Look for parasitized red blood cells.
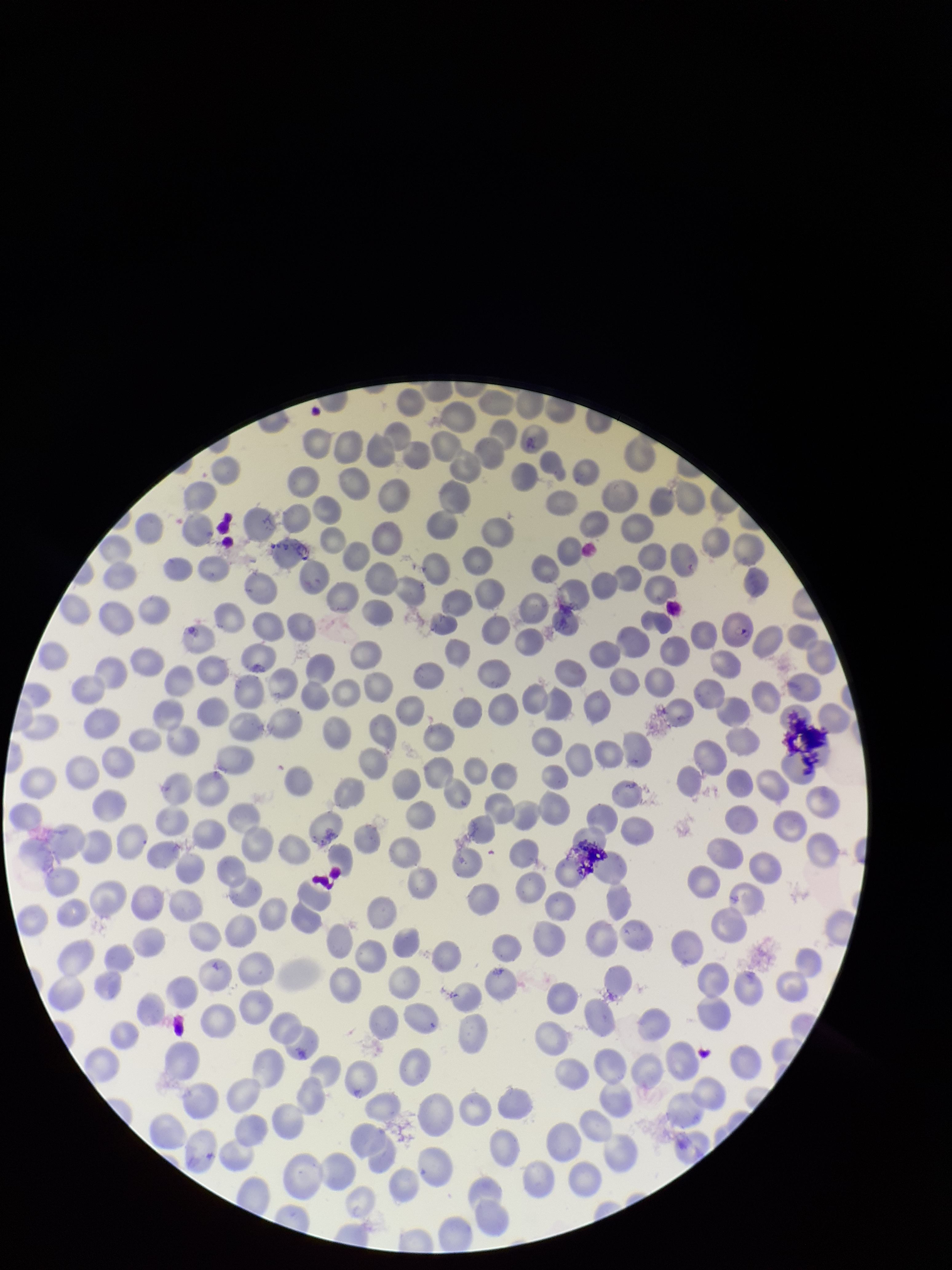

Identified.

{
  "capture": "smartphone photograph through the microscope eyepiece",
  "stain": "Giemsa",
  "field_of_view": "one from this slide",
  "image_size": "952×1270 pixels",
  "red_blood_cell_count": 262,
  "parasitized_red_blood_cell_count": 1,
  "species_reported_for_this_patient": "Plasmodium falciparum",
  "preparation": "thin",
  "patient_malaria_status": "positive"
}